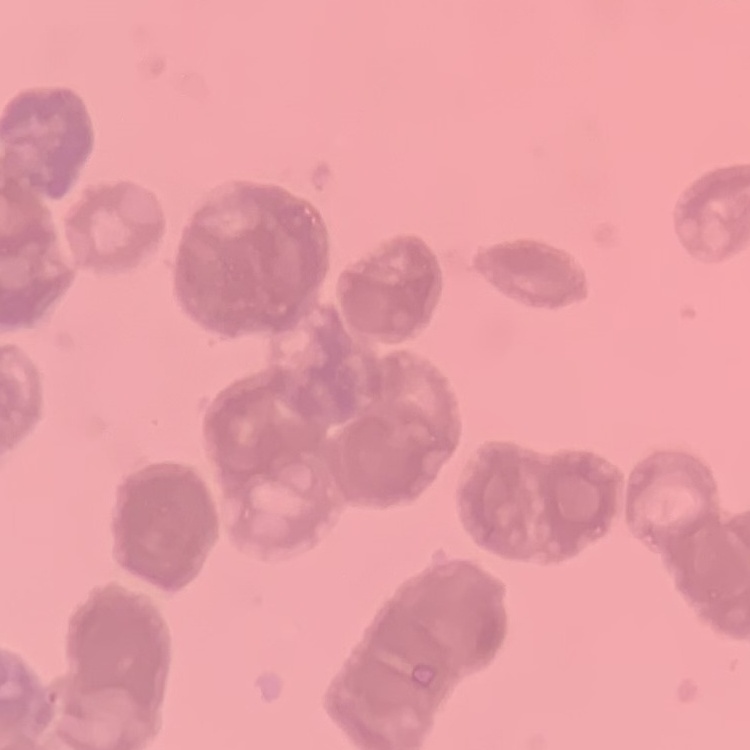

red blood cell morphology = rouleaux formation
image type = square crop of a larger photomicrograph
stain = Field's or Giemsa
preparation = thin blood film